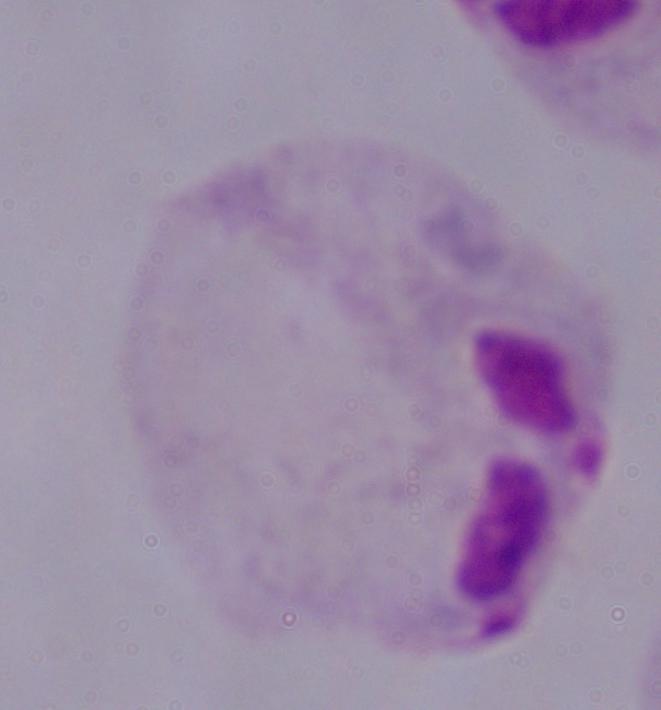
identification: trichomonad
modality: photomicrograph
magnification: 1000x